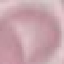

result = negative for malaria parasites
capture = smartphone through the microscope eyepiece
preparation = thin blood smear
image type = automatically extracted cell patch, resized to 64 × 64 pixels
stain = Giemsa